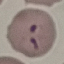

{
  "result": "malaria parasites detected",
  "stain": "Giemsa",
  "preparation": "thin blood smear",
  "image_type": "automatically extracted cell patch, resized to 64 × 64 pixels",
  "capture": "smartphone camera at the microscope eyepiece"
}